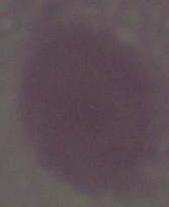

Captured at 1000x magnification. A red blood cell is seen. Micrograph.